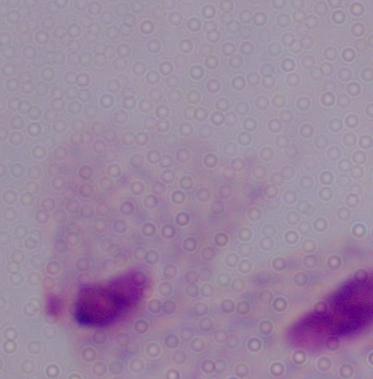

Summary:
  - Modality: photomicrograph
  - Identification: trichomonad
  - Magnification: 1000x